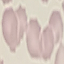

Summary:
  - Malaria status: uninfected
  - Preparation: thin smear
  - Stain: Giemsa
  - Capture: smartphone camera at the microscope eyepiece
  - Image type: automatically extracted cell patch, resized to 64 × 64 pixels